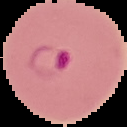
The area outside the segmented cell region is set to black. Result: malaria parasites identified. From a thin blood smear. Image is 127×127 pixels.